Identify the blood parasite species.
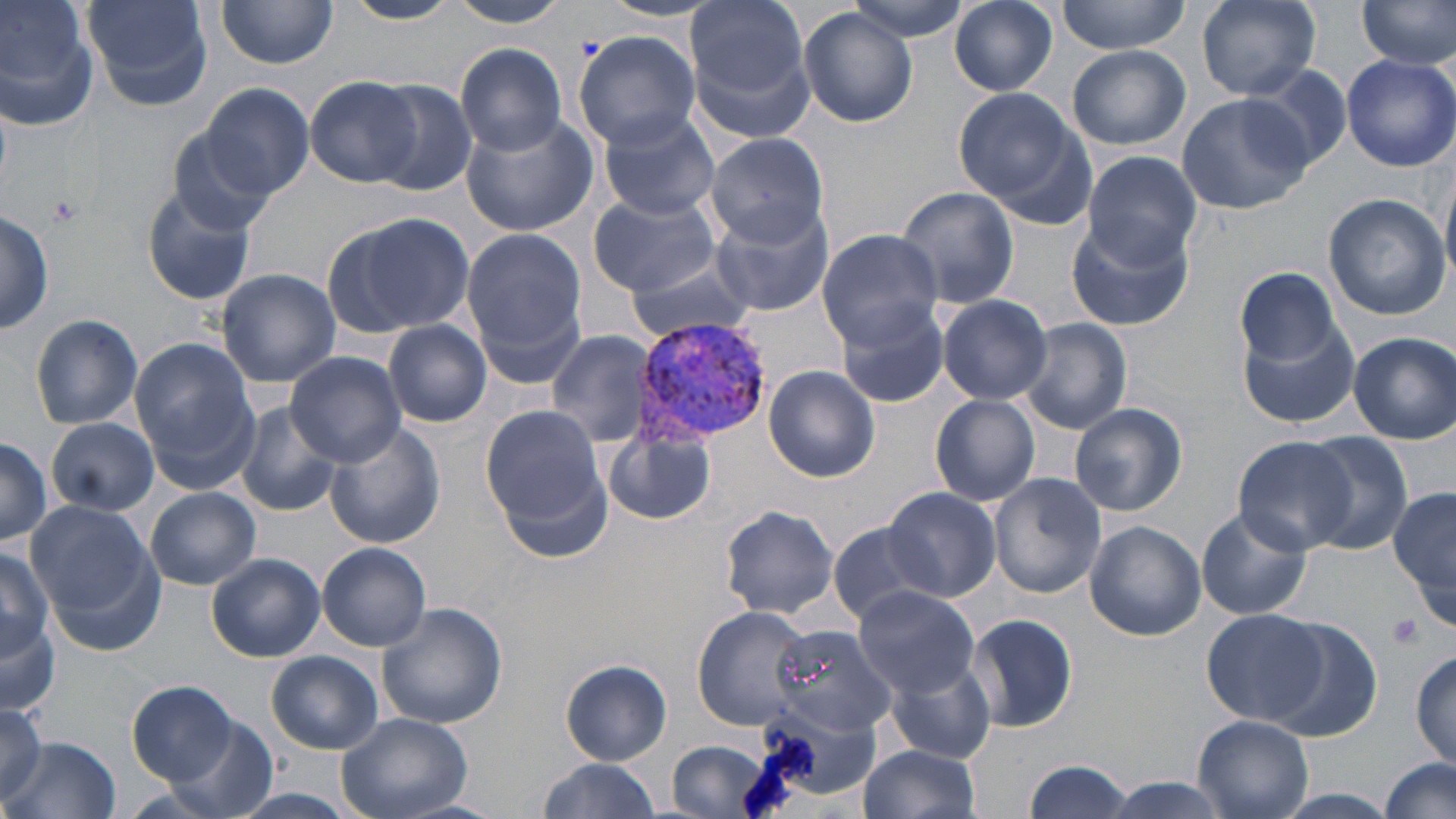
Plasmodium vivax.

uninfected_red_blood_cell_locations: 'approximate bounding boxes as (x1, y1, x2, y2) in pixels: (0, 0, 99, 133), (84, 0, 215, 112), (341, 0, 459, 25), (443, 0, 574, 27), (686, 0, 811, 110), (841, 0, 975, 41), (951, 0, 1058, 96), (1056, 0, 1192, 53), (1355, 0, 1456, 71), (217, 1, 339, 69), (1197, 1, 1321, 99), (798, 8, 919, 127), (572, 32, 700, 148), (455, 42, 568, 154), (1067, 44, 1191, 149), (1341, 53, 1456, 171), (1249, 64, 1353, 173), (305, 76, 421, 186), (363, 79, 480, 196), (199, 82, 315, 200), (953, 87, 1077, 204), (1176, 92, 1316, 214), (597, 108, 722, 219), (170, 110, 294, 229), (461, 112, 597, 238), (704, 132, 830, 246), (1081, 150, 1202, 268), (141, 183, 258, 305), (896, 187, 1023, 312), (587, 191, 722, 297), (1322, 192, 1451, 319), (710, 202, 834, 318), (0, 206, 52, 339), (325, 211, 476, 340), (1065, 217, 1195, 332), (462, 224, 587, 366), (815, 228, 944, 346), (622, 255, 756, 344), (1233, 266, 1345, 368), (216, 270, 341, 385), (936, 293, 1054, 404), (834, 296, 951, 408), (29, 315, 142, 429), (1019, 318, 1131, 433), (383, 321, 495, 426), (1241, 321, 1360, 430), (547, 330, 658, 448), (1349, 331, 1455, 443), (130, 337, 260, 488), (287, 354, 406, 464), (765, 365, 881, 482), (929, 394, 1041, 507), (235, 401, 341, 516), (1070, 403, 1188, 517), (481, 404, 608, 529), (46, 417, 158, 517), (326, 423, 447, 550), (604, 425, 720, 526), (1300, 433, 1414, 553), (0, 436, 50, 545), (1232, 436, 1356, 553), (988, 472, 1105, 598), (883, 485, 1000, 601), (1389, 486, 1455, 612), (146, 488, 260, 589), (27, 503, 162, 647), (717, 506, 841, 618), (1195, 508, 1313, 621), (1083, 520, 1207, 642), (827, 522, 944, 626), (317, 543, 432, 651), (0, 544, 53, 668), (206, 554, 325, 661), (852, 585, 981, 695), (375, 602, 511, 730), (693, 607, 813, 729), (1202, 608, 1329, 726), (965, 612, 1080, 733), (1261, 616, 1382, 738), (0, 624, 60, 713), (771, 624, 899, 737), (265, 650, 385, 755), (1410, 651, 1456, 767), (888, 656, 995, 764), (560, 659, 671, 765), (127, 681, 238, 787), (0, 703, 48, 800), (336, 711, 472, 819), (159, 714, 279, 818), (1192, 714, 1316, 818), (11, 735, 120, 818), (665, 740, 784, 819), (857, 744, 981, 819), (1378, 756, 1455, 819), (535, 759, 663, 817), (1020, 760, 1136, 819), (217, 790, 364, 819)'
platelet_locations: 'approximate bounding boxes as (x1, y1, x2, y2) in pixels: (45, 192, 86, 228), (1386, 612, 1426, 651)'
magnification: 1000x
image_size: 1456×819 pixels
field_of_view: single
stain: May-Grünwald-Giemsa
modality: light microscopy
preparation: thin blood film
plasmodium_vivax_infected_red_blood_cell_locations: 'approximate bounding boxes as (x1, y1, x2, y2) in pixels: (631, 316, 771, 446)'